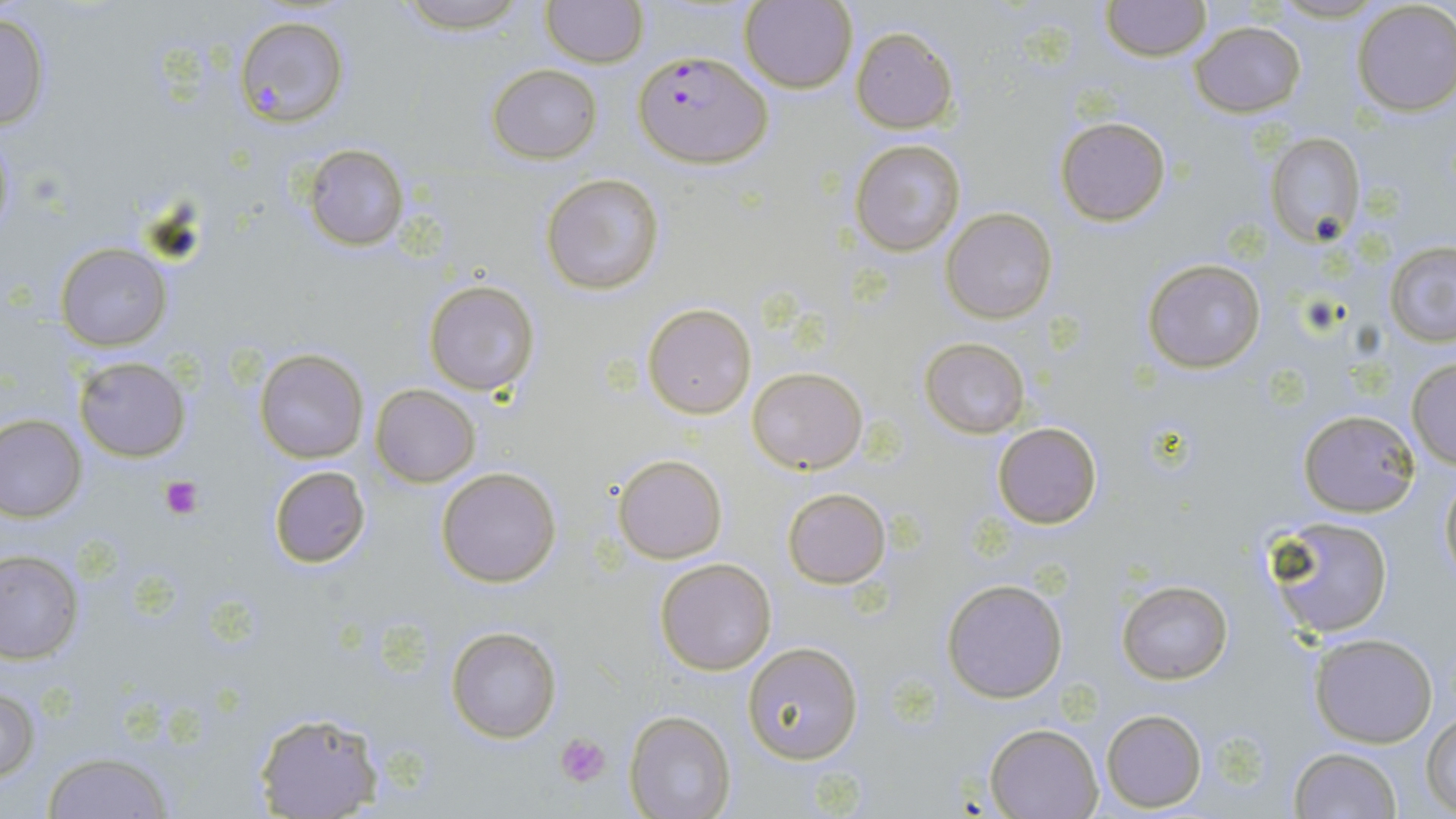
Approximate bounding boxes as [x1, y1, x2, y2] in pixels. Platelet locations: [158, 474, 205, 521], [556, 733, 609, 785]. Plasmodium falciparum-infected red blood cell locations: [635, 51, 771, 167]. Uninfected red blood cell locations: [392, 0, 534, 33], [541, 0, 646, 68], [740, 1, 856, 93], [1101, 1, 1210, 63], [1352, 2, 1456, 116], [0, 10, 51, 132], [234, 15, 349, 128], [1190, 19, 1306, 116], [850, 26, 958, 132], [487, 64, 601, 164], [1055, 116, 1171, 226], [1264, 131, 1365, 246], [850, 137, 966, 258], [301, 143, 409, 251], [541, 172, 665, 295], [941, 207, 1058, 322], [1384, 241, 1456, 346], [56, 243, 172, 351], [1141, 258, 1267, 373], [424, 279, 541, 398], [643, 303, 756, 418], [919, 337, 1029, 438], [255, 349, 370, 464], [73, 356, 191, 461], [1405, 357, 1456, 469], [747, 366, 869, 473], [370, 384, 480, 487], [1298, 409, 1420, 516], [1, 415, 86, 521], [991, 422, 1103, 529], [613, 454, 726, 564], [268, 465, 371, 568], [435, 465, 563, 588], [1439, 469, 1456, 589], [782, 487, 890, 588], [1266, 515, 1394, 641], [1, 549, 81, 664], [655, 557, 778, 676], [941, 577, 1069, 704], [1117, 580, 1232, 685], [446, 625, 562, 743], [1310, 633, 1439, 748], [742, 641, 863, 764], [1, 686, 41, 783], [1100, 709, 1207, 812], [252, 710, 385, 819], [626, 711, 736, 819], [1422, 712, 1456, 814], [985, 723, 1102, 818], [1288, 748, 1402, 819], [41, 752, 176, 819]. Slide-level diagnosis: Plasmodium falciparum. Thin blood smear. May-Grünwald-Giemsa stain. Single field of view. Optical microscopy. 1000x magnification. Image is 1456×819 pixels.